Report the malaria status of this cell.
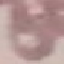
It is uninfected.

Giemsa-stained preparation. Automatically extracted cell patch, resized to 64 × 64 pixels. Thin blood smear. Acquired by smartphone through the microscope eyepiece.